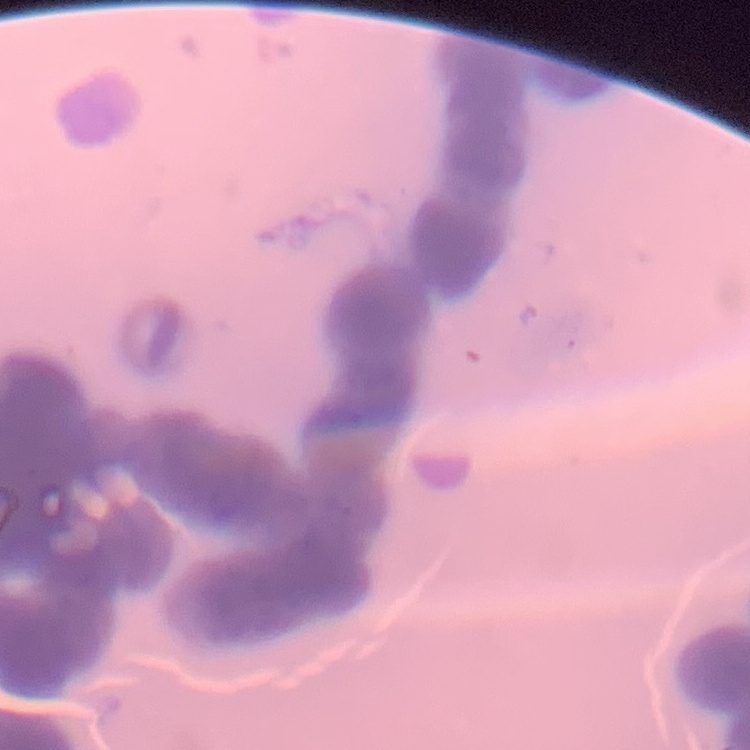
{
  "red_blood_cell_morphology": "rouleaux formation",
  "stain": "Field's or Giemsa",
  "preparation": "thin blood film",
  "image_type": "one tile cut from a larger photomicrograph"
}